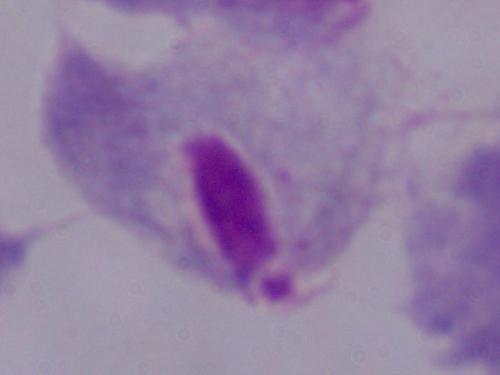

modality = micrograph
identification = trichomonad
magnification = 1000x